Report the malaria status of this cell.
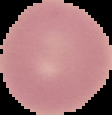

Uninfected.

Segmented cell region on a black background. Image is 112×115 pixels. From a thin blood film.